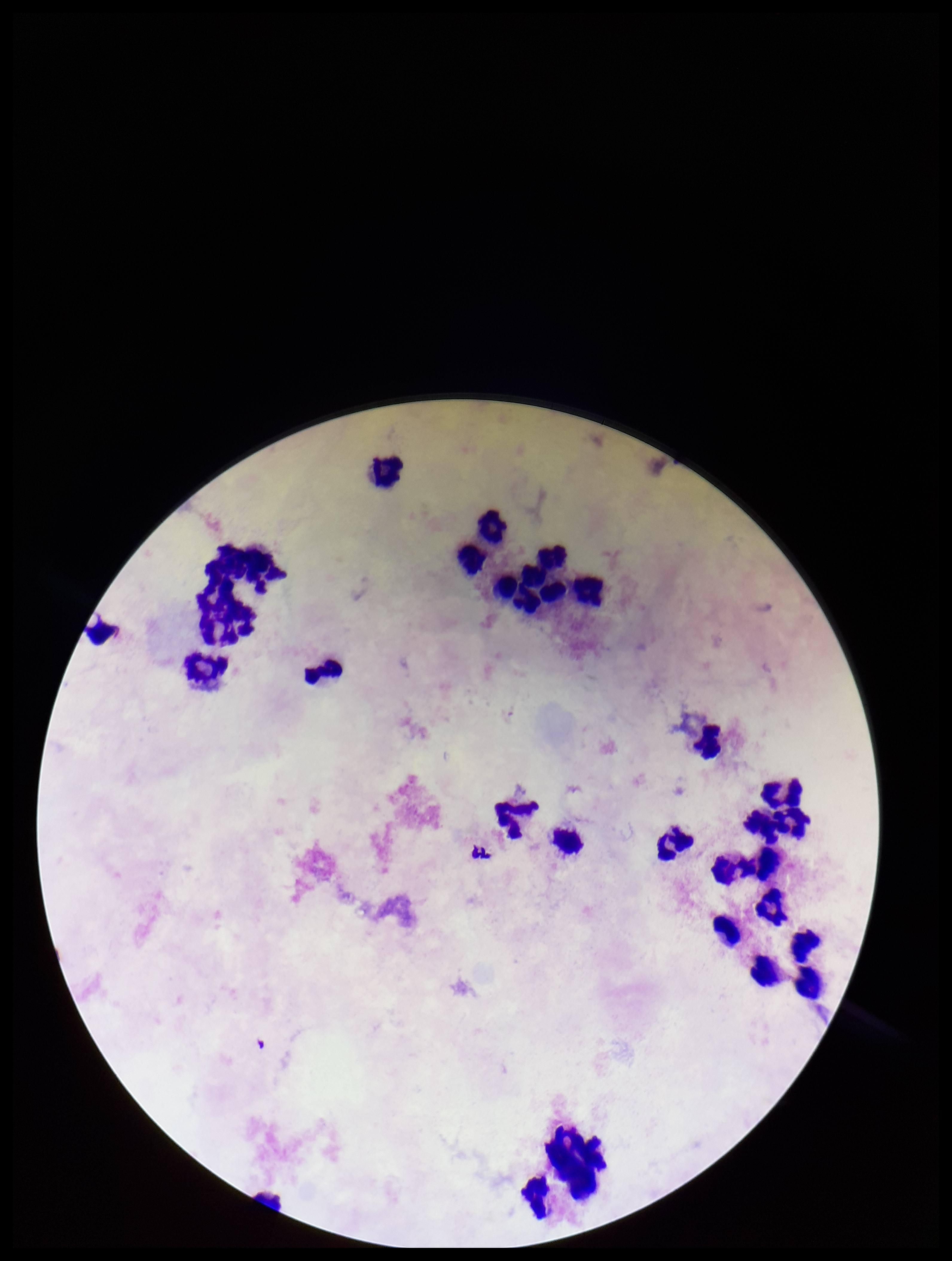
Summary:
  - Capture: smartphone photograph through the microscope eyepiece
  - Patient malaria status: negative
  - Field of view: single
  - Leukocyte count: 28
  - Plasmodium parasites: none seen
  - Stain: Giemsa
  - Preparation: thick blood smear
  - Image size: 952×1261 pixels
  - Parasite count: 0